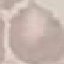

Summary:
  - Result: no malaria parasites seen
  - Image type: cell patch, automatically extracted from a larger field of view and resized to 64 × 64 pixels
  - Stain: Giemsa
  - Capture: smartphone camera at the microscope eyepiece
  - Preparation: thin smear